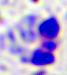

Summary:
  - Modality: micrograph
  - Identification: leukocyte
  - Magnification: 400x